State which cell type is depicted.
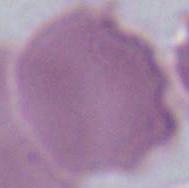

This is an erythrocyte.

modality = photomicrograph
magnification = 1000x